Classify this cell by malaria status.
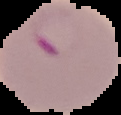
It is parasitized.

Image is 121×115 pixels. From a thin blood smear. The area outside the segmented cell region is set to black.